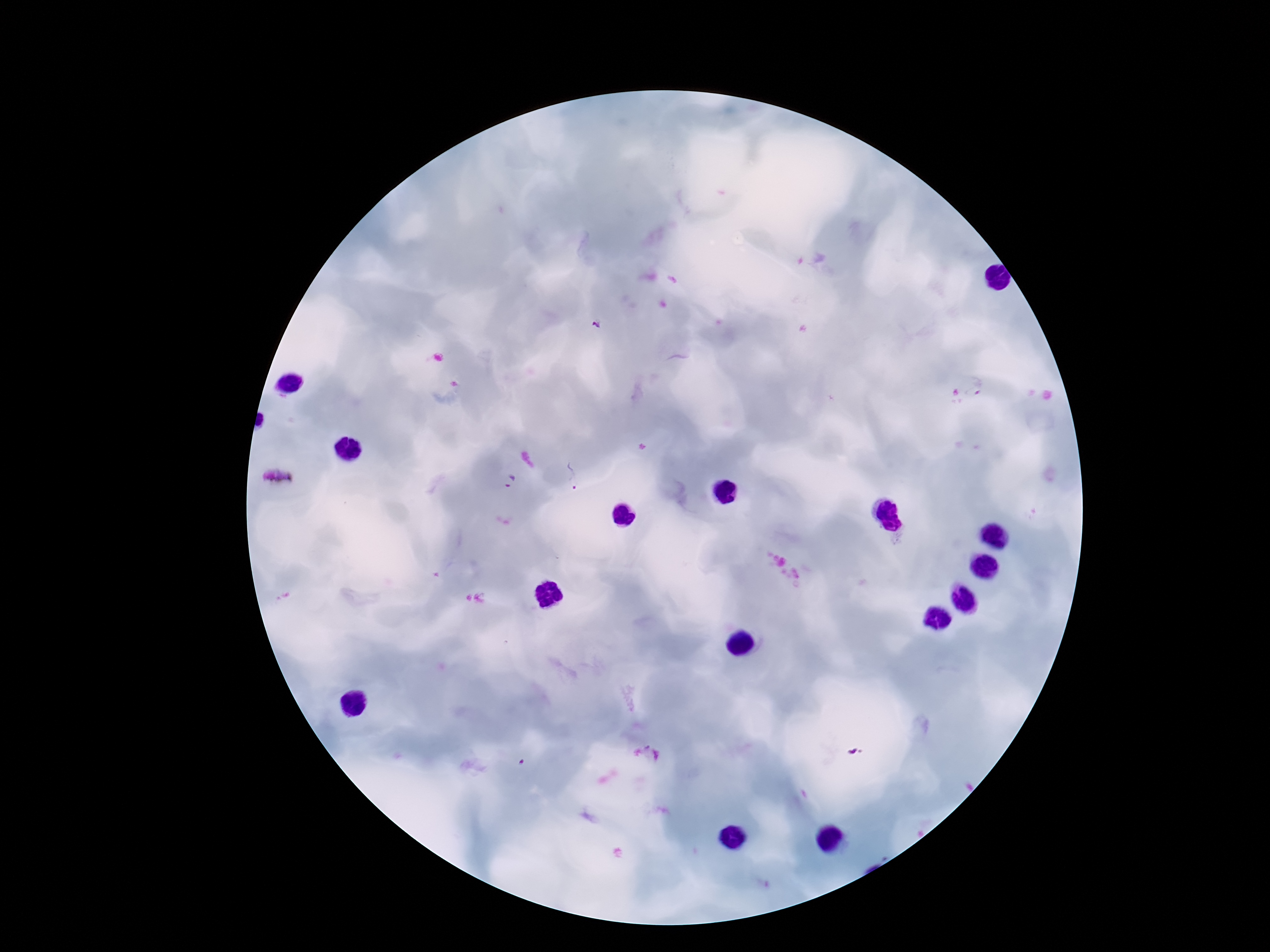

preparation: thick blood smear
stain: Giemsa
plasmodium_parasite_locations: 'approximate centers as [x, y] in pixels: [596, 324], [980, 385], [575, 475], [278, 480], [511, 481]'
magnification: 100x
image_size: 1270×952 pixels
field_of_view: single
patient_malaria_status: infected
capture: smartphone camera through the microscope eyepiece